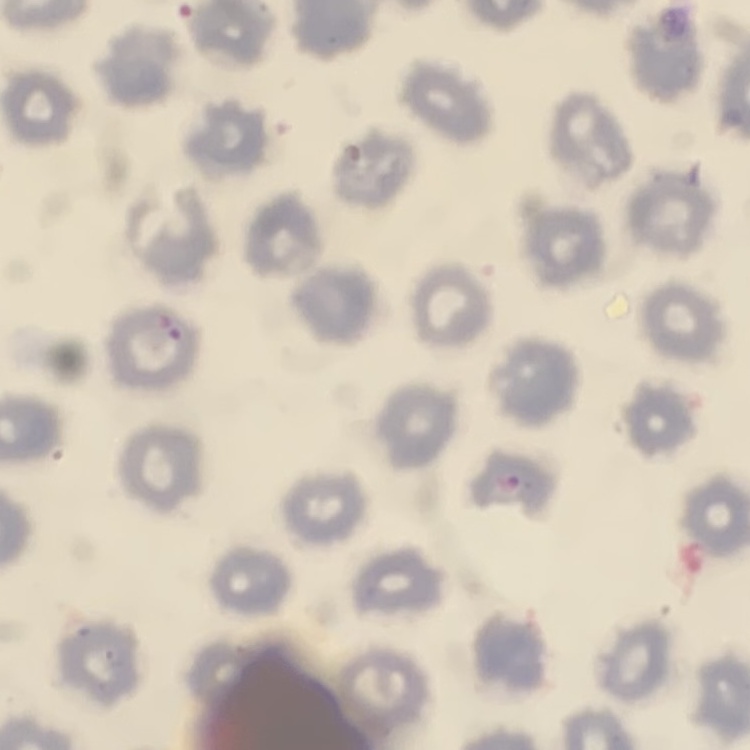
Summary:
  - Red blood cell morphology: no rouleaux formation
  - Stain: Field's or Giemsa
  - Preparation: thin blood film
  - Image type: one tile cut from a larger photomicrograph